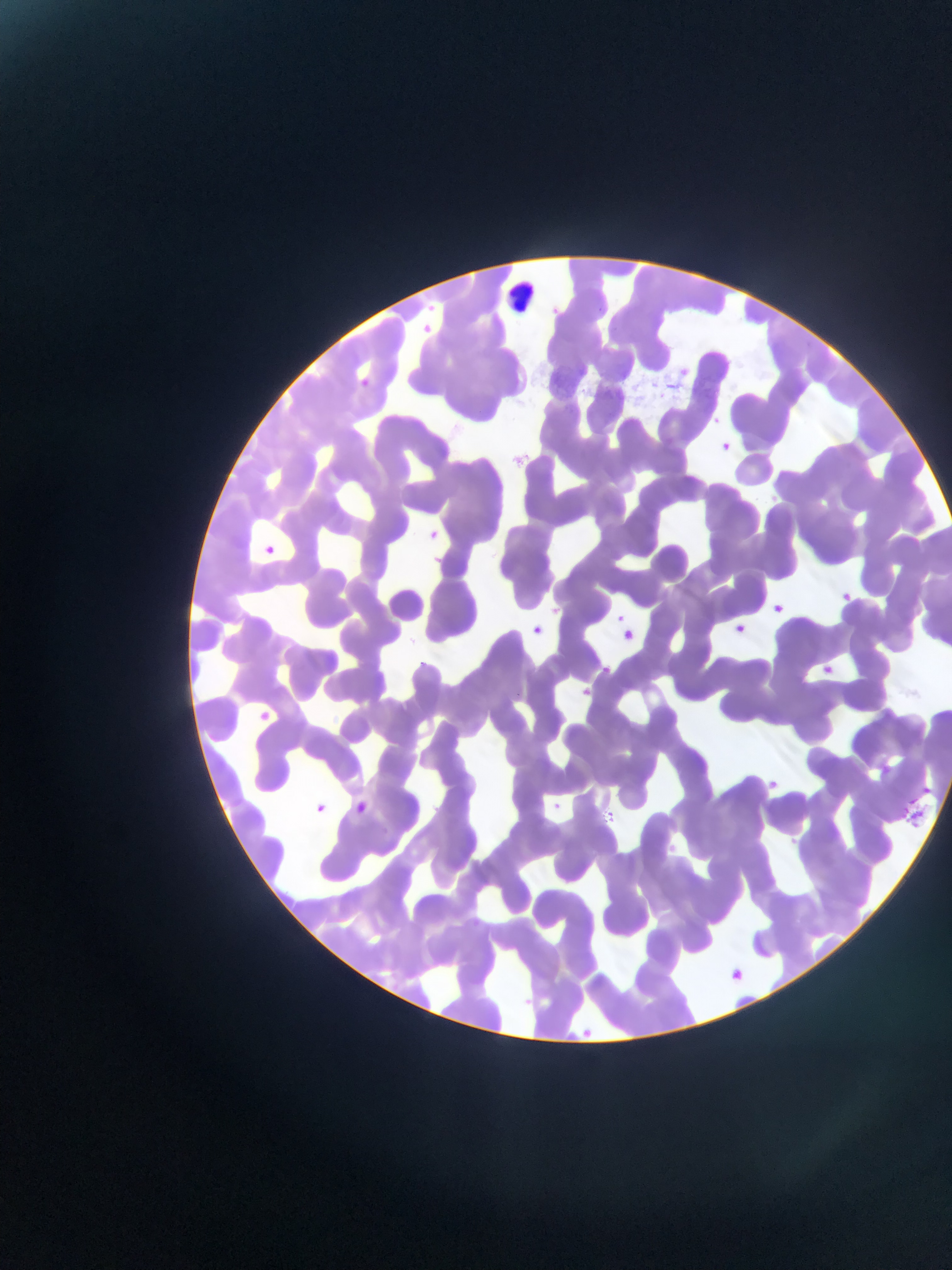

Approximate bounding boxes as {left, top, right, bottom} in pixels.
Summary:
  - Leukocyte locations: {500, 275, 563, 320}
  - Plasmodium parasite locations: {413, 319, 440, 343}, {349, 373, 375, 397}, {708, 414, 725, 427}, {718, 441, 734, 455}, {713, 443, 735, 460}, {514, 450, 533, 465}, {424, 525, 445, 544}, {257, 542, 280, 563}, {838, 590, 854, 605}, {769, 600, 786, 617}, {547, 604, 564, 619}, {612, 610, 629, 626}, {609, 616, 634, 637}, {731, 621, 748, 636}, {528, 623, 544, 638}, {619, 627, 637, 644}, {414, 657, 429, 672}, {818, 662, 837, 678}, {578, 685, 594, 700}, {252, 706, 275, 728}, {878, 757, 893, 778}, {765, 777, 780, 791}, {350, 798, 371, 817}, {548, 798, 565, 813}, {309, 800, 331, 819}, {904, 807, 927, 829}, {602, 810, 618, 824}, {665, 841, 680, 855}, {723, 964, 752, 980}
  - Image size: 952×1270 pixels
  - Field of view: single
  - Capture: mobile-phone photograph through a microscope
  - Preparation: thin blood film
  - Country: Ghana